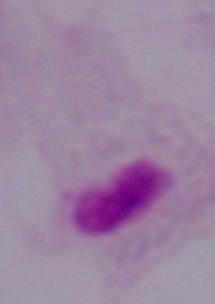
identification = trichomonad
modality = micrograph
magnification = 1000x